Assess this cell for malaria.
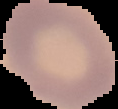
It is uninfected.

From a thin blood film. Image is 118×109 pixels. The area outside the segmented cell region is set to black.